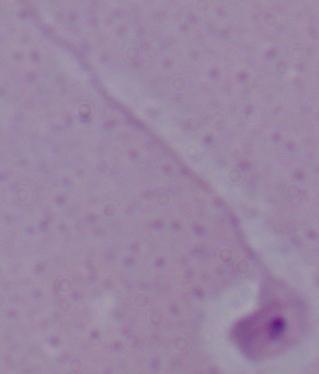

modality = photomicrograph
identification = Leishmania
magnification = 1000x